Name the parasite shown.
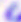

Toxoplasma gondii.

Micrograph. Captured at 400x magnification.